Report the malaria status of this cell.
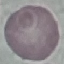
It is uninfected.

stain: Giemsa
preparation: thin blood film
image_type: cell patch, automatically extracted from a larger field of view and resized to 64 × 64 pixels
capture: smartphone camera at the microscope eyepiece